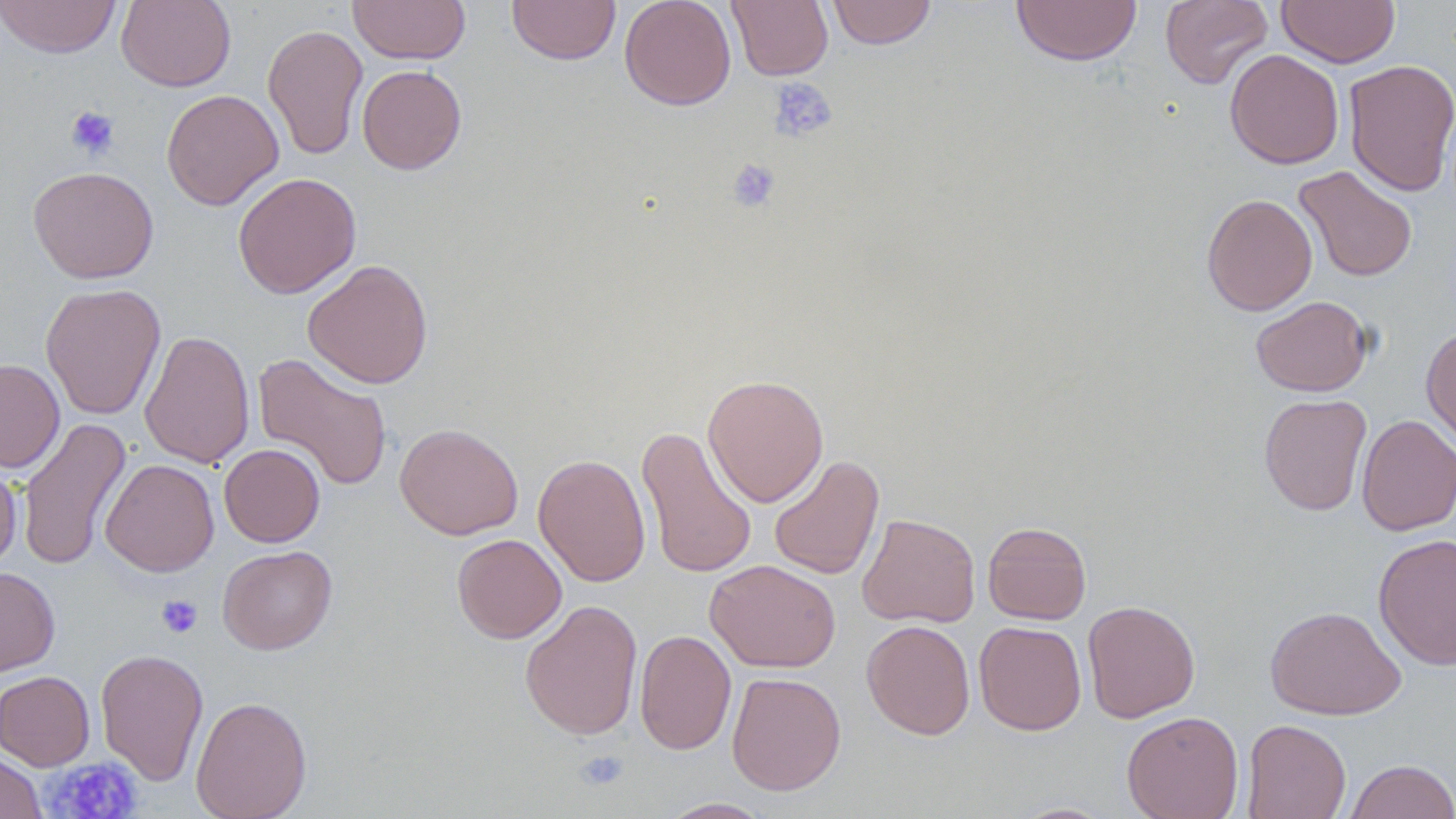

Summary:
  - Coordinate format: approximate bounding boxes as named x1/y1/x2/y2 corners in pixels
  - Uninfected red blood cell locations: (x1=0, y1=0, x2=122, y2=58), (x1=116, y1=0, x2=236, y2=91), (x1=347, y1=0, x2=471, y2=65), (x1=506, y1=0, x2=620, y2=65), (x1=619, y1=0, x2=736, y2=110), (x1=727, y1=0, x2=833, y2=81), (x1=826, y1=0, x2=937, y2=49), (x1=1010, y1=0, x2=1142, y2=66), (x1=1160, y1=0, x2=1273, y2=89), (x1=1276, y1=0, x2=1400, y2=67), (x1=262, y1=24, x2=369, y2=161), (x1=1224, y1=49, x2=1344, y2=169), (x1=1343, y1=59, x2=1456, y2=197), (x1=357, y1=65, x2=466, y2=174), (x1=161, y1=89, x2=284, y2=211), (x1=1293, y1=165, x2=1418, y2=282), (x1=28, y1=166, x2=159, y2=284), (x1=232, y1=172, x2=362, y2=299), (x1=1201, y1=193, x2=1318, y2=316), (x1=303, y1=259, x2=434, y2=389), (x1=40, y1=283, x2=166, y2=420), (x1=1250, y1=296, x2=1373, y2=396), (x1=1421, y1=325, x2=1456, y2=450), (x1=139, y1=329, x2=256, y2=469), (x1=253, y1=353, x2=394, y2=491), (x1=0, y1=358, x2=65, y2=473), (x1=702, y1=374, x2=829, y2=507), (x1=1259, y1=393, x2=1372, y2=516), (x1=1356, y1=414, x2=1456, y2=536), (x1=16, y1=416, x2=132, y2=571), (x1=395, y1=423, x2=523, y2=540), (x1=636, y1=425, x2=758, y2=581), (x1=219, y1=443, x2=325, y2=547), (x1=533, y1=453, x2=651, y2=587), (x1=768, y1=454, x2=885, y2=580), (x1=100, y1=459, x2=219, y2=577), (x1=0, y1=460, x2=21, y2=572), (x1=857, y1=513, x2=980, y2=628), (x1=981, y1=521, x2=1092, y2=624), (x1=452, y1=533, x2=567, y2=643), (x1=1372, y1=533, x2=1456, y2=671), (x1=217, y1=545, x2=337, y2=654), (x1=705, y1=559, x2=841, y2=673), (x1=0, y1=566, x2=60, y2=676), (x1=520, y1=599, x2=643, y2=740), (x1=1082, y1=600, x2=1200, y2=723), (x1=1265, y1=605, x2=1406, y2=720), (x1=861, y1=619, x2=975, y2=740), (x1=974, y1=621, x2=1087, y2=735), (x1=634, y1=629, x2=736, y2=755), (x1=95, y1=648, x2=209, y2=785), (x1=0, y1=670, x2=95, y2=770), (x1=726, y1=671, x2=846, y2=796), (x1=190, y1=696, x2=312, y2=819), (x1=1121, y1=711, x2=1244, y2=819), (x1=1241, y1=719, x2=1351, y2=819), (x1=0, y1=751, x2=46, y2=819), (x1=1345, y1=759, x2=1456, y2=819), (x1=658, y1=797, x2=774, y2=818), (x1=1010, y1=801, x2=1118, y2=819)
  - Platelet locations: (x1=767, y1=77, x2=838, y2=143), (x1=65, y1=106, x2=120, y2=161), (x1=726, y1=158, x2=781, y2=213), (x1=156, y1=595, x2=203, y2=639), (x1=573, y1=749, x2=630, y2=792), (x1=42, y1=757, x2=143, y2=818)
  - Slide-level diagnosis: negative for blood parasites
  - Magnification: 1000x
  - Field of view: single
  - Preparation: thin blood smear
  - Stain: May-Grünwald-Giemsa
  - Image size: 1456×819 pixels
  - Modality: optical microscopy